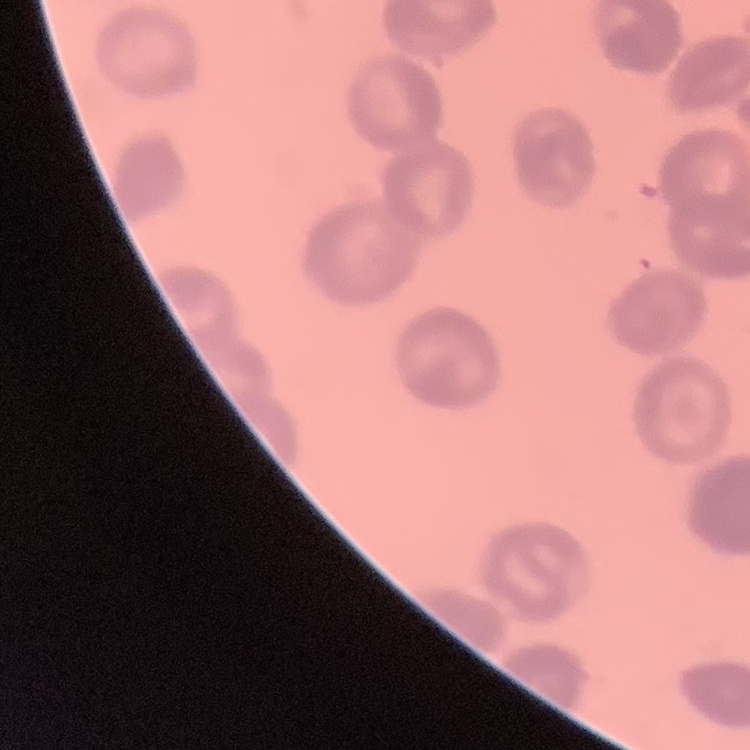

Summary:
  - Red blood cell morphology: rouleaux formation
  - Image type: square crop of a larger photomicrograph
  - Preparation: thin blood smear
  - Stain: Field's or Giemsa